Locate every white blood cell.
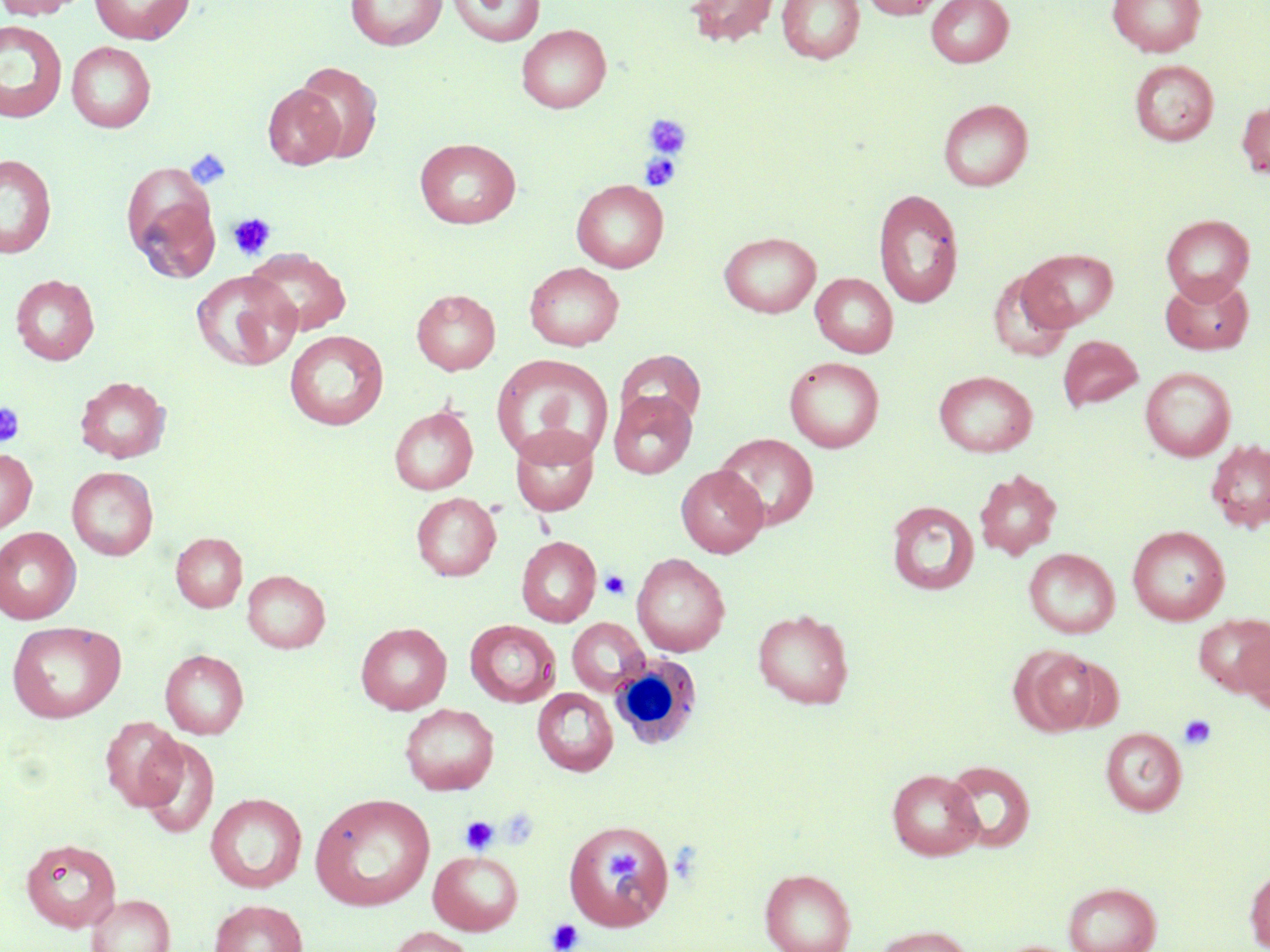

Approximate bounding boxes as (x1, y1, x2, y2) in pixels.
White blood cells: (609, 653, 703, 750).

slide-level diagnosis = negative for blood parasites
uninfected red blood cell locations = approximate bounding boxes as (x1, y1, x2, y2) in pixels: (0, 0, 85, 19), (90, 0, 194, 45), (345, 0, 447, 50), (448, 0, 545, 47), (684, 0, 780, 47), (777, 0, 865, 64), (860, 0, 949, 19), (926, 0, 1014, 67), (1107, 0, 1207, 57), (0, 19, 68, 124), (516, 24, 611, 113), (66, 41, 156, 132), (1130, 60, 1219, 146), (295, 62, 383, 162), (264, 83, 345, 170), (938, 99, 1032, 191), (1236, 100, 1270, 179), (415, 137, 521, 229), (0, 154, 57, 258), (122, 163, 220, 281), (571, 179, 668, 273), (873, 188, 965, 308), (1161, 214, 1255, 302), (718, 231, 822, 318), (245, 247, 352, 336), (1020, 248, 1118, 330), (524, 262, 624, 350), (987, 269, 1075, 362), (190, 270, 302, 371), (811, 273, 898, 358), (1160, 273, 1254, 355), (11, 274, 100, 365), (411, 289, 501, 374), (284, 330, 389, 430), (1058, 334, 1143, 411), (615, 349, 706, 430), (491, 354, 614, 465), (784, 356, 885, 452), (1140, 367, 1236, 461), (934, 370, 1038, 457), (75, 376, 170, 463), (608, 390, 697, 479), (389, 405, 478, 495), (509, 426, 600, 516), (714, 433, 819, 531), (1206, 439, 1270, 532), (0, 448, 37, 533), (676, 465, 768, 557), (67, 466, 158, 560), (974, 468, 1062, 560), (411, 492, 501, 581), (887, 500, 979, 595), (1128, 525, 1230, 625), (0, 527, 81, 623), (171, 532, 247, 612), (516, 536, 601, 627), (1024, 548, 1120, 638), (632, 553, 730, 656), (242, 570, 330, 653), (753, 609, 854, 709), (1194, 614, 1270, 696), (567, 618, 649, 695), (6, 620, 126, 723), (464, 620, 561, 708), (355, 622, 452, 715), (1238, 627, 1270, 714), (1012, 647, 1107, 735), (160, 649, 248, 739), (532, 688, 618, 776), (399, 703, 499, 795), (100, 718, 188, 810), (1100, 727, 1187, 815), (138, 737, 219, 838), (943, 760, 1036, 852), (887, 768, 983, 860), (206, 792, 307, 893), (311, 793, 434, 911), (562, 823, 675, 933), (21, 837, 122, 932), (428, 850, 523, 935), (1245, 865, 1270, 951), (759, 868, 857, 952), (1063, 882, 1161, 952), (88, 894, 175, 952), (209, 899, 308, 952), (872, 925, 973, 952), (384, 926, 477, 952)
image size = 1270×952 pixels
preparation = thin blood smear
platelet locations = approximate bounding boxes as (x1, y1, x2, y2) in pixels: (643, 114, 692, 159), (184, 148, 232, 191), (639, 153, 682, 191), (227, 212, 277, 260), (0, 402, 25, 447), (600, 570, 630, 599), (1178, 714, 1217, 751), (460, 816, 498, 854), (603, 849, 643, 883), (547, 918, 584, 952)
field of view = single
modality = light microscopy
stain = May-Grünwald-Giemsa
magnification = 1000x